Outline each blood parasite and name the species.
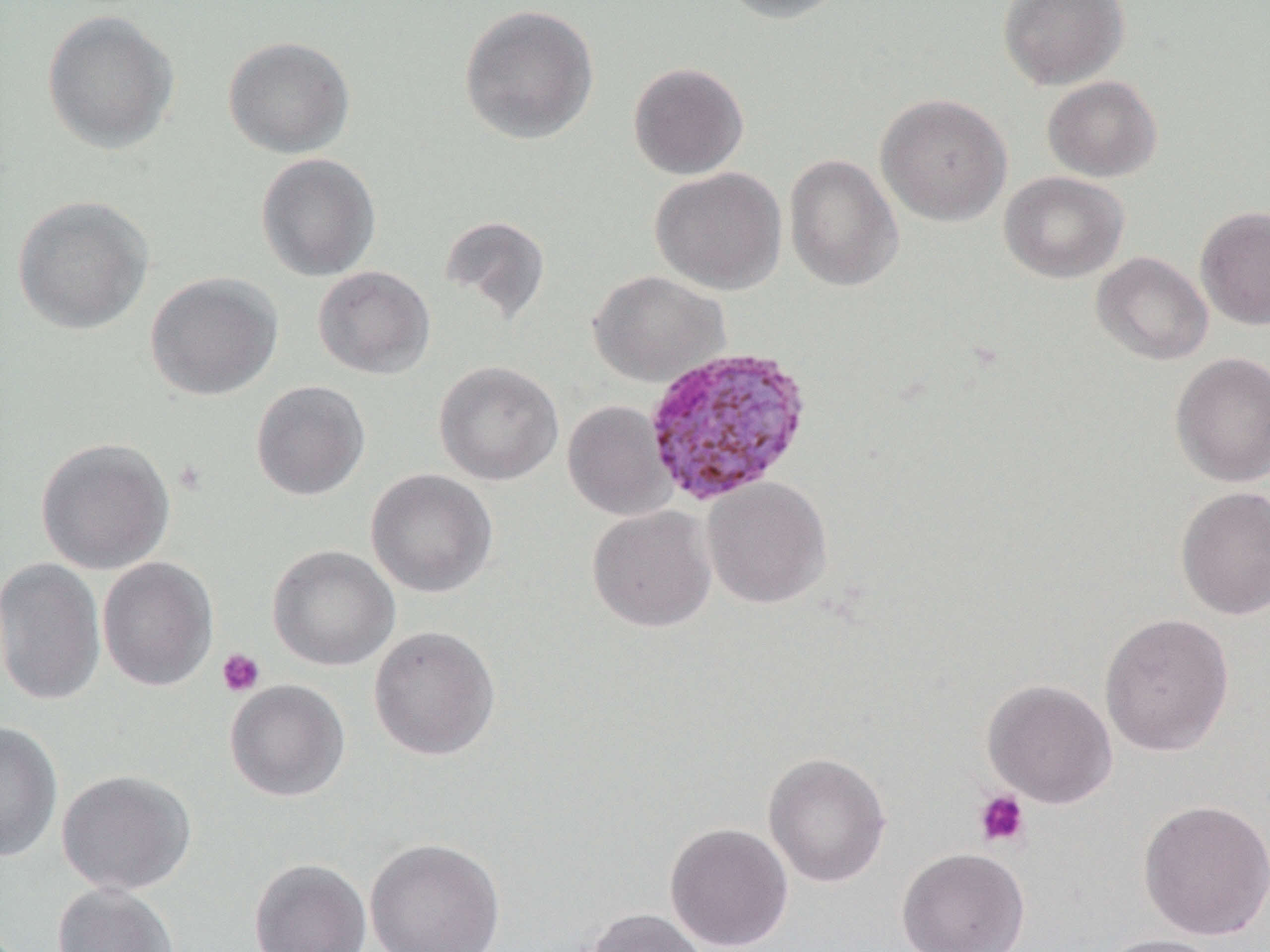
Approximate bounding boxes as [x1, y1, x2, y2] in pixels.
Plasmodium ovale-infected red blood cells: [643, 345, 813, 506].
No Plasmodium falciparum, Plasmodium malariae, Plasmodium vivax, Babesia divergens, or Trypanosoma brucei observed.

Summary:
  - Platelet locations: [216, 648, 266, 697], [973, 789, 1030, 848]
  - Uninfected red blood cell locations: [716, 0, 854, 24], [998, 0, 1129, 90], [457, 4, 600, 145], [41, 10, 180, 155], [223, 35, 355, 158], [628, 61, 749, 180], [1042, 75, 1163, 182], [875, 93, 1012, 227], [255, 152, 381, 282], [784, 154, 904, 292], [650, 167, 786, 295], [999, 171, 1129, 283], [12, 196, 154, 335], [1195, 206, 1270, 330], [439, 214, 552, 326], [1091, 251, 1213, 365], [313, 266, 435, 379], [588, 270, 729, 387], [145, 272, 283, 401], [1170, 352, 1270, 487], [434, 361, 564, 486], [251, 380, 370, 501], [562, 400, 675, 521], [35, 437, 175, 575], [365, 469, 498, 598], [702, 477, 832, 609], [1175, 486, 1270, 620], [587, 505, 717, 632], [267, 545, 400, 671], [0, 557, 106, 707], [97, 557, 218, 692], [1098, 612, 1235, 756], [368, 625, 501, 761], [981, 678, 1117, 809], [225, 679, 350, 802], [0, 721, 63, 863], [763, 752, 892, 888], [56, 769, 197, 896], [1137, 798, 1270, 941], [664, 822, 794, 951], [364, 837, 506, 951], [896, 847, 1030, 952], [249, 858, 371, 952], [51, 883, 180, 952], [584, 907, 710, 952], [1097, 933, 1230, 952]
  - Slide-level diagnosis: Plasmodium ovale
  - Image size: 1270×952 pixels
  - Magnification: 1000x
  - Field of view: single
  - Preparation: thin blood film
  - Modality: light microscopy